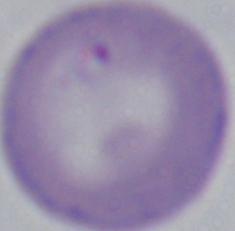

Photomicrograph. 1000x magnification. A Babesia parasite is shown.